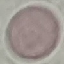
Summary:
  - Malaria status: uninfected
  - Stain: Giemsa
  - Preparation: thin smear
  - Image type: cell patch, automatically extracted from a larger field of view and resized to 64 × 64 pixels
  - Capture: smartphone through the microscope eyepiece